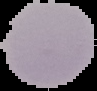
image_size: 97×91 pixels
image_type: cell region segmented out of the field of view; surrounding area masked to black
preparation: thin blood smear
malaria_status: uninfected